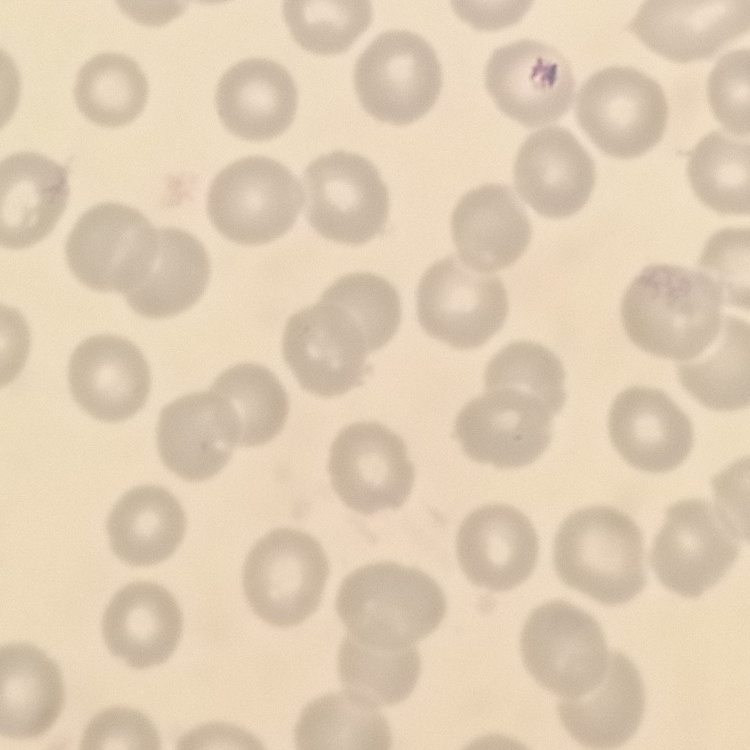
Summary:
  - Red blood cell morphology: no rouleaux formation
  - Image type: one tile cut from a larger photomicrograph
  - Stain: Field's or Giemsa
  - Preparation: thin blood film